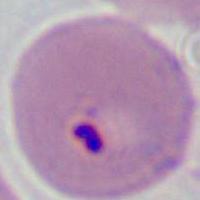

magnification = 400x or 1000x
modality = micrograph
identification = Plasmodium